Locate every blood parasite and identify its species.
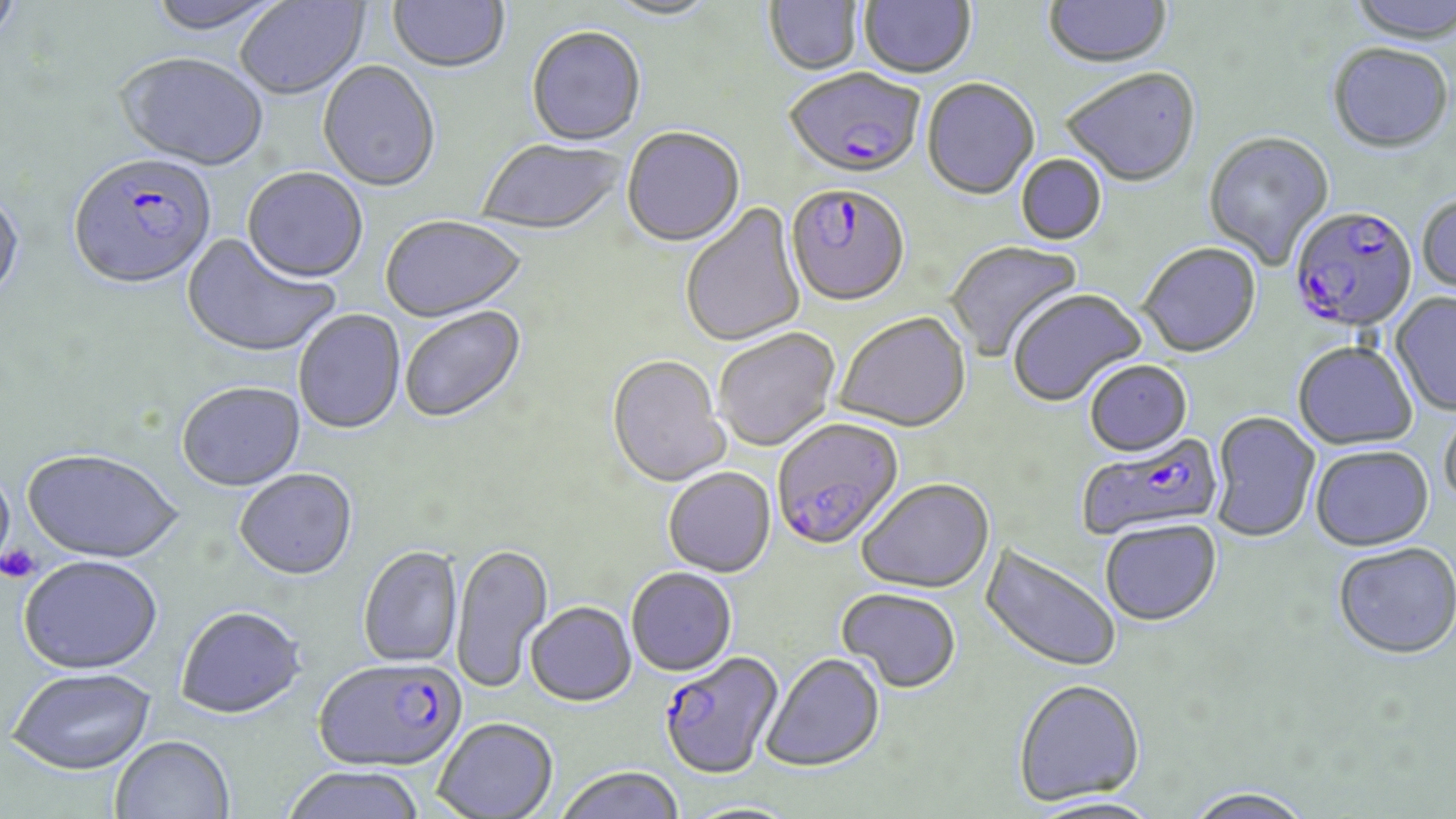

Approximate bounding boxes as (x1,y1)-(x2,y2) corner pairs in pixels.
Plasmodium falciparum-infected red blood cells: (785,70)-(925,182), (68,156)-(217,293), (785,186)-(910,309), (1289,207)-(1417,336), (772,419)-(905,552), (1076,434)-(1224,541), (660,651)-(785,780), (313,658)-(467,772).
No Plasmodium ovale, Plasmodium malariae, Plasmodium vivax, Babesia divergens, or Trypanosoma brucei observed.

slide-level diagnosis = Plasmodium falciparum
image size = 1456×819 pixels
preparation = thin blood smear
uninfected red blood cell locations = approximate bounding boxes as (x1,y1)-(x2,y2) corner pairs in pixels: (0,0)-(26,55), (143,0)-(290,37), (235,0)-(369,102), (388,0)-(509,75), (764,0)-(864,77), (858,0)-(976,81), (1349,0)-(1456,47), (602,1)-(722,23), (1042,1)-(1173,72), (526,28)-(646,149), (1327,44)-(1453,156), (115,54)-(269,173), (318,63)-(441,194), (1062,70)-(1201,190), (921,80)-(1040,202), (622,128)-(745,249), (1204,133)-(1335,270), (477,141)-(626,236), (1016,154)-(1107,246), (241,169)-(368,286), (0,191)-(26,309), (1416,195)-(1456,299), (679,201)-(807,348), (380,217)-(527,324), (181,234)-(341,360), (945,239)-(1084,363), (1138,244)-(1262,360), (1008,289)-(1147,408), (1389,293)-(1456,417), (400,307)-(528,425), (293,310)-(406,435), (834,314)-(971,435), (714,329)-(840,452), (1292,343)-(1417,451), (607,357)-(731,489), (1084,362)-(1192,458), (177,383)-(306,492), (1439,408)-(1456,514), (1209,413)-(1320,544), (1310,447)-(1434,553), (22,450)-(184,565), (0,463)-(15,579), (234,469)-(358,581), (663,469)-(776,578), (856,480)-(995,594), (1100,521)-(1222,629), (980,541)-(1121,675), (452,543)-(554,693), (1333,545)-(1456,663), (358,546)-(464,669), (19,556)-(163,675), (626,568)-(737,678), (836,589)-(961,695), (525,603)-(636,707), (175,605)-(307,719), (761,654)-(885,773), (7,667)-(157,776), (1013,680)-(1145,807), (434,718)-(558,818), (110,735)-(235,819), (282,766)-(425,819), (556,766)-(685,819), (1181,787)-(1316,819), (681,802)-(802,819)
platelet locations = approximate bounding boxes as (x1,y1)-(x2,y2) corner pairs in pixels: (0,545)-(39,583)
stain = May-Grünwald-Giemsa
modality = optical microscopy
field of view = one of a larger specimen
magnification = 1000x